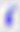
Photomicrograph. Toxoplasma gondii is shown. Captured at 400x magnification.